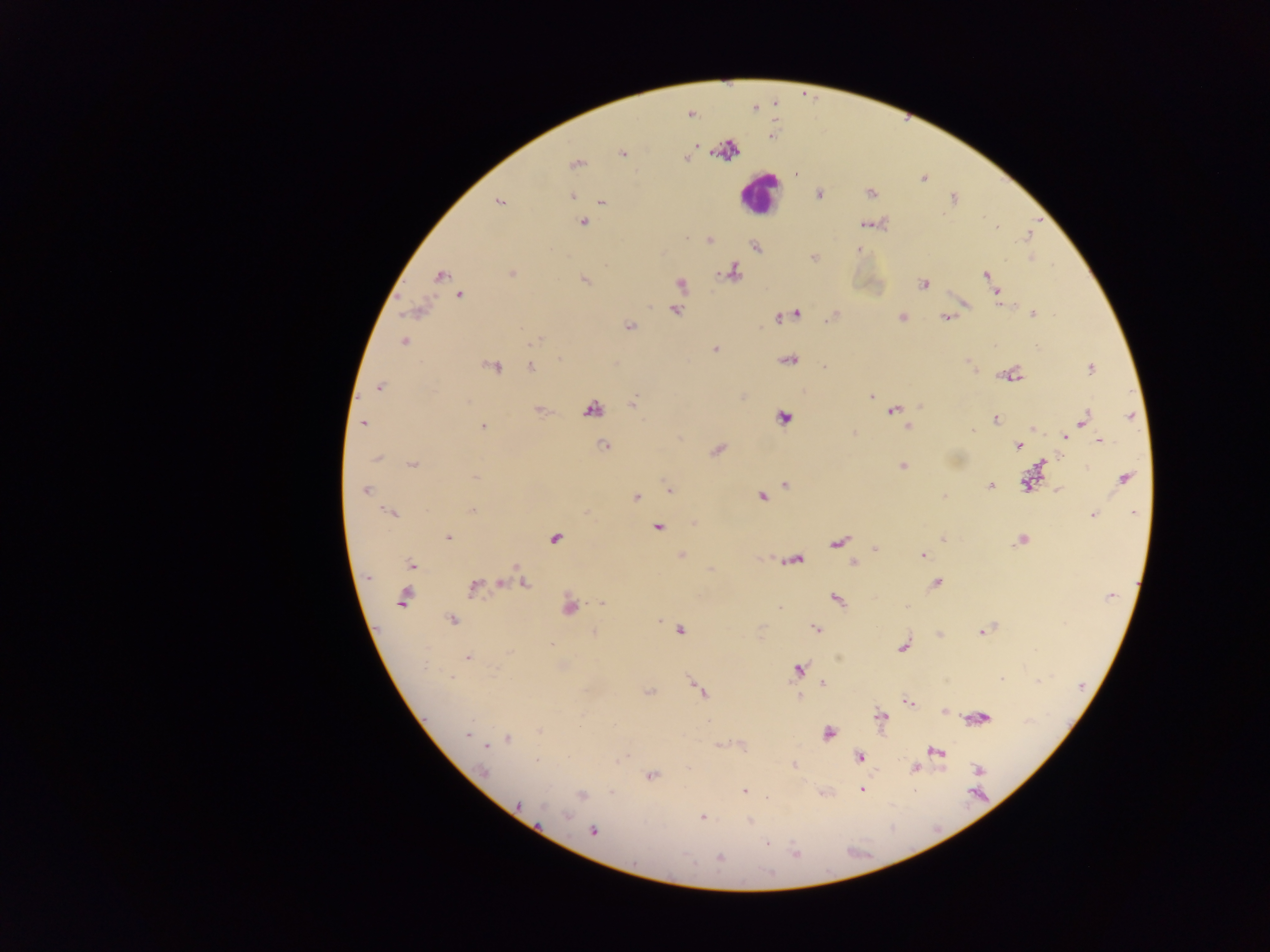
image size = 1270×952 pixels
country = Ghana
field of view = single
preparation = thick blood film
leukocyte locations = approximate centers as {x, y} in pixels: {759, 193}
malaria parasite locations = approximate centers as {x, y} in pixels: {622, 154}, {686, 159}, {575, 165}, {796, 173}, {819, 193}, {870, 193}, {572, 196}, {953, 198}, {499, 201}, {601, 202}, {584, 223}, {864, 224}, {997, 227}, {1028, 236}, {710, 240}, {755, 246}, {858, 250}, {814, 257}, {733, 272}, {512, 273}, {986, 274}, {440, 275}, {584, 279}, {990, 281}, {680, 284}, {923, 284}, {997, 293}, {459, 296}, {676, 310}, {796, 313}, {1033, 314}, {901, 318}, {946, 318}, {782, 319}, {630, 326}, {536, 340}, {403, 342}, {714, 350}, {559, 360}, {789, 361}, {493, 366}, {825, 366}, {531, 368}, {1090, 369}, {1014, 375}, {379, 388}, {871, 397}, {633, 403}, {919, 407}, {591, 409}, {893, 410}, {540, 411}, {1130, 417}, {782, 418}, {996, 419}, {1084, 419}, {363, 423}, {482, 427}, {907, 427}, {1033, 428}, {971, 430}, {1065, 438}, {1100, 441}, {603, 446}, {1018, 446}, {716, 451}, {376, 460}, {413, 464}, {1042, 465}, {902, 466}, {475, 477}, {1124, 478}, {1026, 482}, {785, 484}, {990, 485}, {670, 490}, {1058, 490}, {365, 491}, {761, 496}, {636, 497}, {472, 510}, {389, 513}, {1134, 513}, {1093, 515}, {657, 528}, {447, 537}, {555, 538}, {943, 538}, {1021, 541}, {838, 542}, {876, 548}, {922, 555}, {681, 556}, {795, 560}, {852, 563}, {411, 565}, {501, 583}, {937, 583}, {524, 584}, {474, 587}, {1111, 596}, {402, 598}, {837, 600}, {602, 603}, {569, 607}, {780, 608}, {452, 620}, {659, 621}, {816, 628}, {680, 630}, {982, 631}, {594, 633}, {940, 635}, {550, 644}, {903, 646}, {509, 652}, {468, 657}, {798, 669}, {450, 677}, {1002, 679}, {1039, 681}, {823, 684}, {699, 690}, {649, 692}, {908, 701}, {944, 711}, {881, 716}, {983, 718}, {540, 731}, {828, 733}, {467, 734}, {508, 738}, {487, 746}, {936, 752}, {859, 757}, {537, 760}, {795, 765}, {914, 768}, {979, 769}, {483, 771}, {651, 775}, {862, 790}, {744, 791}, {612, 792}, {582, 795}, {520, 804}, {565, 816}, {701, 817}, {751, 821}, {593, 831}, {767, 843}, {795, 853}, {720, 857}, {771, 874}
capture = mobile-phone photograph through a microscope